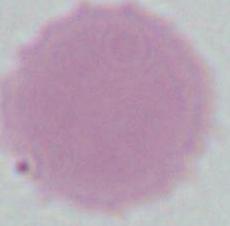
identification: red blood cell
magnification: 1000x
modality: photomicrograph